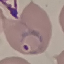
Summary:
  - Result: malaria parasites identified
  - Capture: smartphone camera at the microscope eyepiece
  - Stain: Giemsa
  - Preparation: thin blood smear
  - Image type: cell patch, automatically extracted from a larger field of view and resized to 64 × 64 pixels